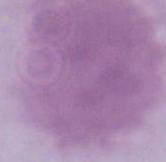

magnification = 1000x
modality = photomicrograph
identification = red blood cell